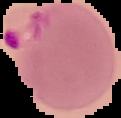
image_type: segmented cell region on a black background
result: Plasmodium parasites detected
image_size: 121×118 pixels
preparation: thin blood film